State which parasite is depicted.
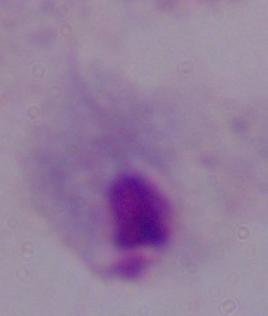
This is a trichomonad.

1000x magnification. Photomicrograph.